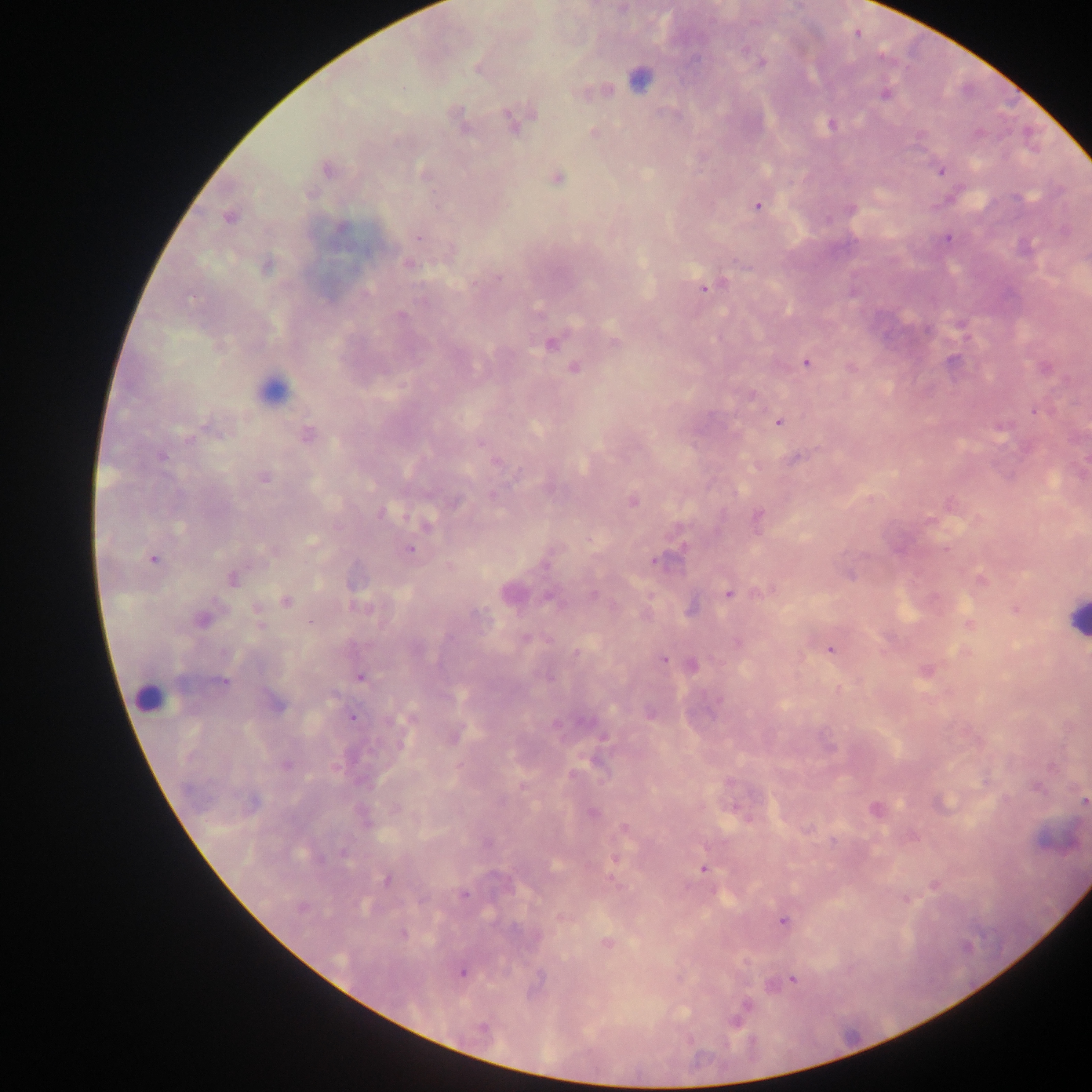

Approximate centers as (x, y) in pixels. Malaria parasite locations: (762, 63), (884, 94), (512, 120), (831, 125), (462, 126), (594, 134), (328, 170), (941, 171), (423, 173), (558, 178), (1018, 197), (757, 206), (229, 217), (342, 229), (418, 238), (947, 239), (409, 264), (265, 267), (704, 289), (400, 315), (550, 343), (615, 343), (806, 363), (574, 368), (752, 396), (1034, 411), (779, 423), (307, 435), (188, 439), (481, 443), (160, 456), (796, 459), (496, 462), (264, 478), (632, 501), (455, 502), (381, 513), (758, 516), (930, 520), (426, 524), (311, 541), (409, 549), (153, 559), (656, 561), (849, 575), (234, 579), (980, 579), (728, 594), (593, 595), (286, 602), (359, 607), (1015, 610), (202, 619), (259, 620), (310, 623), (970, 624), (526, 638), (738, 643), (830, 650), (576, 653), (663, 660), (692, 664), (925, 671), (360, 676), (223, 682), (274, 702), (353, 717), (401, 743), (286, 765), (1038, 787), (1084, 800), (593, 813), (625, 828), (344, 853), (617, 858), (703, 868), (387, 879), (935, 885), (464, 894), (301, 907), (782, 922), (403, 935), (607, 943), (462, 972), (793, 978), (746, 1007), (735, 1020), (482, 1028). Leukocyte locations: (636, 78), (273, 389), (1075, 617), (148, 697). Sample from Ghana. Thick blood film. Photographed through a microscope with a mobile-phone camera. Image is 1092×1092 pixels. Single field of view.